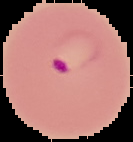

malaria status = parasitized
preparation = thin blood smear
image size = 133×142 pixels
image type = cell region segmented out of the field of view; surrounding area masked to black